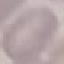

result = no malaria parasites detected
image type = automatically extracted cell patch, resized to 64 × 64 pixels
capture = smartphone camera at the microscope eyepiece
preparation = thin blood smear
stain = Giemsa